Classify this cell by malaria status.
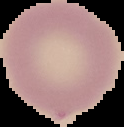
Uninfected.

image size = 124×127 pixels
preparation = thin blood film
image type = segmented cell region with the area outside set to black